Assess this cell for malaria.
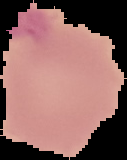

Uninfected.

image type = segmented cell region with the area outside set to black
preparation = thin blood smear
image size = 127×160 pixels